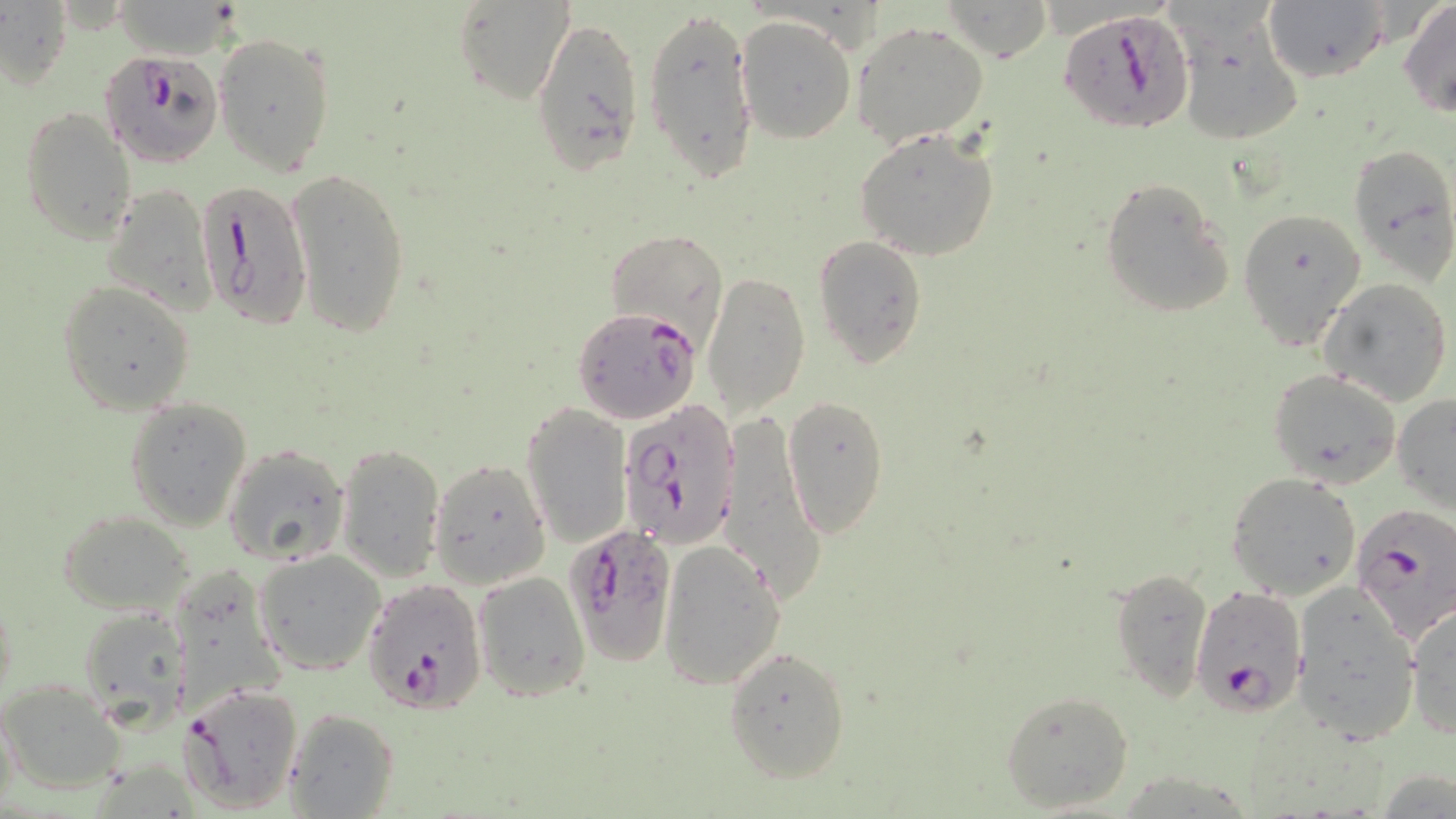
Summary:
  - Coordinate format: approximate bounding boxes as [x1, y1, x2, y2] in pixels
  - Plasmodium falciparum-infected red blood cell locations: [1060, 7, 1194, 134], [102, 50, 222, 167], [196, 176, 313, 332], [574, 309, 702, 424], [617, 399, 739, 549], [1349, 506, 1455, 652], [564, 524, 676, 664], [362, 578, 486, 712], [1190, 585, 1308, 716], [180, 682, 303, 812]
  - Uninfected red blood cell locations: [453, 0, 575, 108], [940, 0, 1050, 62], [1399, 0, 1456, 118], [1, 2, 71, 89], [110, 2, 239, 61], [1262, 2, 1390, 84], [644, 3, 760, 183], [529, 12, 646, 179], [736, 14, 857, 144], [852, 21, 989, 148], [1181, 23, 1304, 147], [215, 32, 337, 174], [21, 106, 136, 243], [855, 127, 1000, 260], [1347, 141, 1456, 283], [286, 166, 411, 339], [1099, 176, 1235, 320], [102, 183, 216, 315], [1236, 206, 1365, 348], [606, 228, 729, 347], [813, 236, 926, 366], [702, 272, 810, 419], [1320, 278, 1452, 406], [57, 280, 196, 415], [1267, 370, 1400, 489], [781, 393, 890, 539], [1393, 394, 1456, 513], [126, 396, 252, 530], [521, 401, 631, 547], [721, 408, 824, 606], [336, 443, 444, 581], [223, 444, 351, 566], [429, 458, 552, 587], [1228, 473, 1361, 601], [59, 510, 196, 617], [659, 539, 786, 689], [254, 550, 386, 675], [167, 567, 287, 720], [1108, 567, 1213, 703], [472, 571, 590, 701], [1291, 582, 1421, 744], [1407, 601, 1456, 739], [77, 607, 190, 729], [723, 644, 851, 783], [2, 680, 125, 792], [999, 688, 1135, 813], [283, 706, 399, 818]
  - Slide-level diagnosis: Plasmodium falciparum
  - Preparation: thin blood film
  - Modality: light microscopy
  - Field of view: single
  - Magnification: 1000x
  - Image size: 1456×819 pixels
  - Stain: May-Grünwald-Giemsa